Identify the parasite.
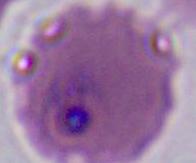
Plasmodium.

400x or 1000x magnification. Photomicrograph.